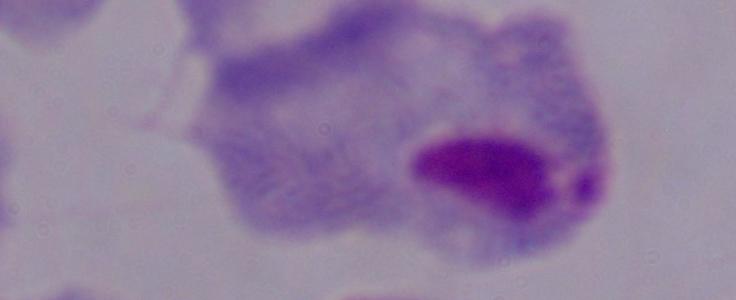
Summary:
  - Magnification: 1000x
  - Identification: trichomonad
  - Modality: photomicrograph